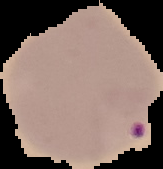

Image is 163×169 pixels. Segmented cell region on a black background. Malaria status: parasitized. From a thin blood smear.